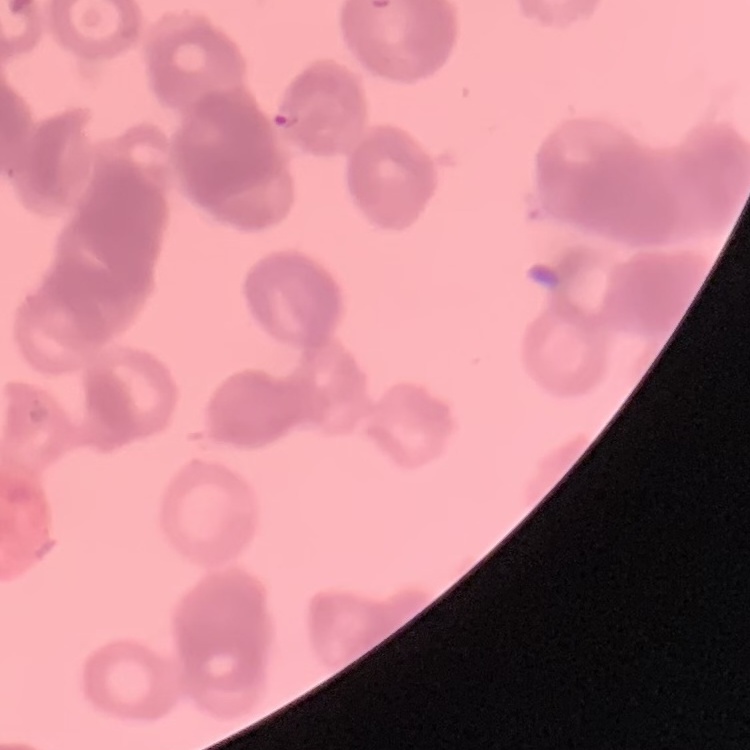
The erythrocytes show rouleaux formation. Field's or Giemsa stain. Thin blood smear. Square crop of a larger photomicrograph.